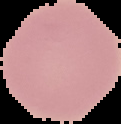 Segmented cell region on a black background. Result: no malaria parasites detected. From a thin blood film. Image is 121×124 pixels.